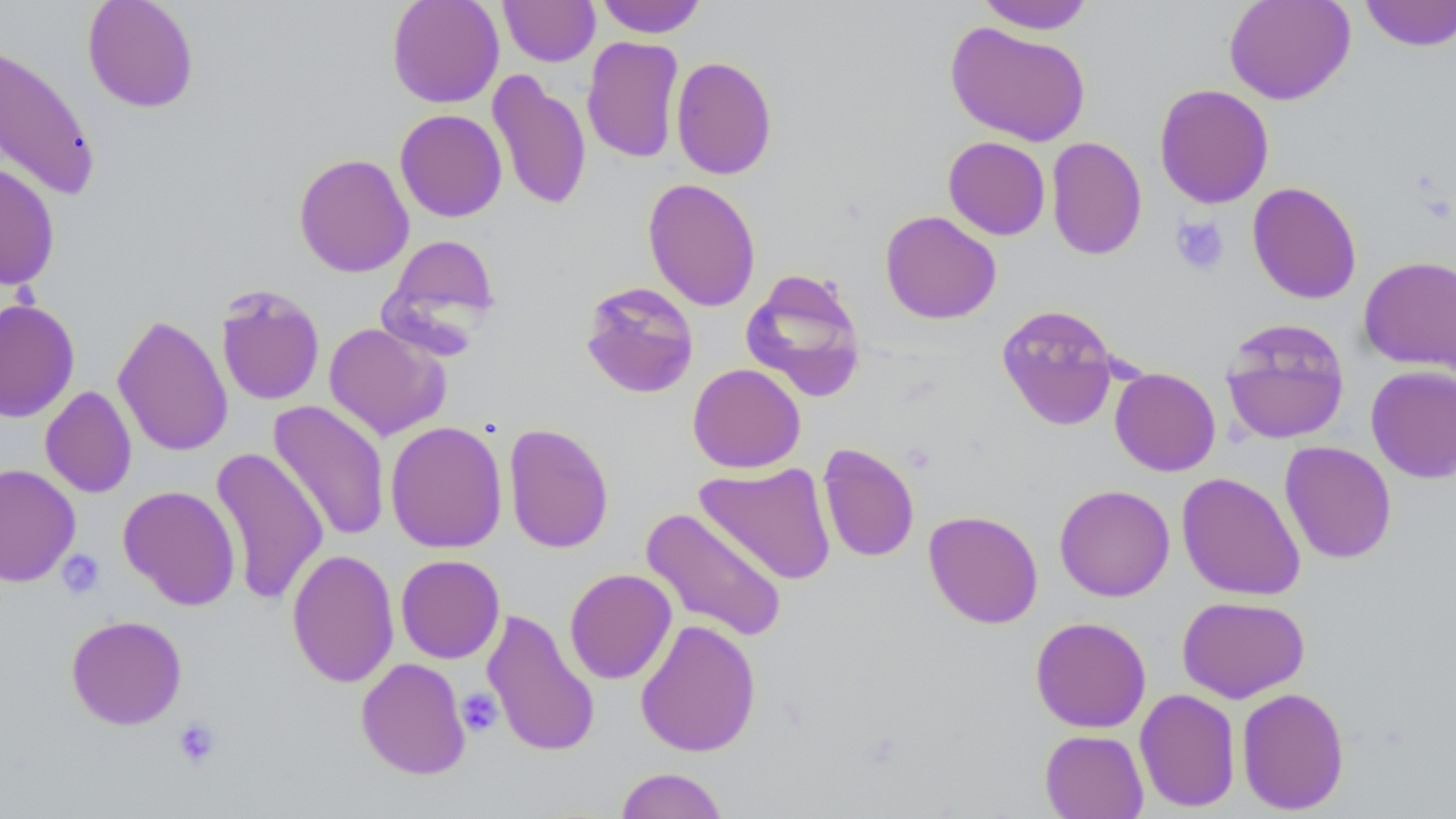

Summary:
  - Coordinate format: approximate bounding boxes as (x1,y1)-(x2,y2) corner pairs in pixels
  - Uninfected red blood cell locations: (82,0)-(200,113), (386,0)-(505,108), (499,0)-(600,67), (594,0)-(708,37), (1223,0)-(1355,105), (1360,0)-(1456,52), (975,1)-(1096,34), (945,22)-(1091,146), (582,36)-(684,163), (0,43)-(102,202), (671,56)-(778,180), (487,70)-(591,211), (1154,83)-(1274,209), (395,109)-(507,222), (943,136)-(1051,240), (1046,136)-(1147,261), (293,153)-(414,278), (0,160)-(60,290), (642,177)-(761,312), (1247,182)-(1362,304), (880,210)-(1002,324), (381,234)-(502,344), (1359,256)-(1456,374), (740,267)-(867,404), (579,280)-(700,399), (215,285)-(325,406), (0,297)-(80,423), (996,303)-(1120,430), (112,313)-(233,457), (1219,318)-(1351,445), (323,322)-(451,441), (687,363)-(806,473), (1365,365)-(1456,483), (1109,367)-(1220,476), (40,386)-(137,498), (268,400)-(391,542), (385,420)-(508,553), (503,423)-(614,554), (1279,441)-(1397,564), (817,443)-(920,563), (209,447)-(329,605), (694,461)-(837,585), (0,463)-(81,587), (1177,472)-(1305,601), (1054,484)-(1175,601), (118,485)-(241,611), (639,507)-(788,643), (923,510)-(1044,629), (286,548)-(399,688), (395,554)-(505,663), (564,568)-(677,684), (1177,596)-(1310,703), (481,609)-(600,758), (66,615)-(187,730), (1030,616)-(1152,733), (635,618)-(761,757), (355,657)-(471,780), (1236,687)-(1350,815), (1134,688)-(1241,813), (1039,729)-(1149,818), (614,767)-(729,818)
  - Platelet locations: (1170,215)-(1230,275), (56,549)-(106,599), (456,688)-(503,737), (172,718)-(221,770)
  - Slide-level diagnosis: no evidence of blood parasites
  - Field of view: single
  - Preparation: thin blood film
  - Stain: May-Grünwald-Giemsa
  - Modality: optical microscopy
  - Image size: 1456×819 pixels
  - Magnification: 1000x